Locate every uninfected red blood cell.
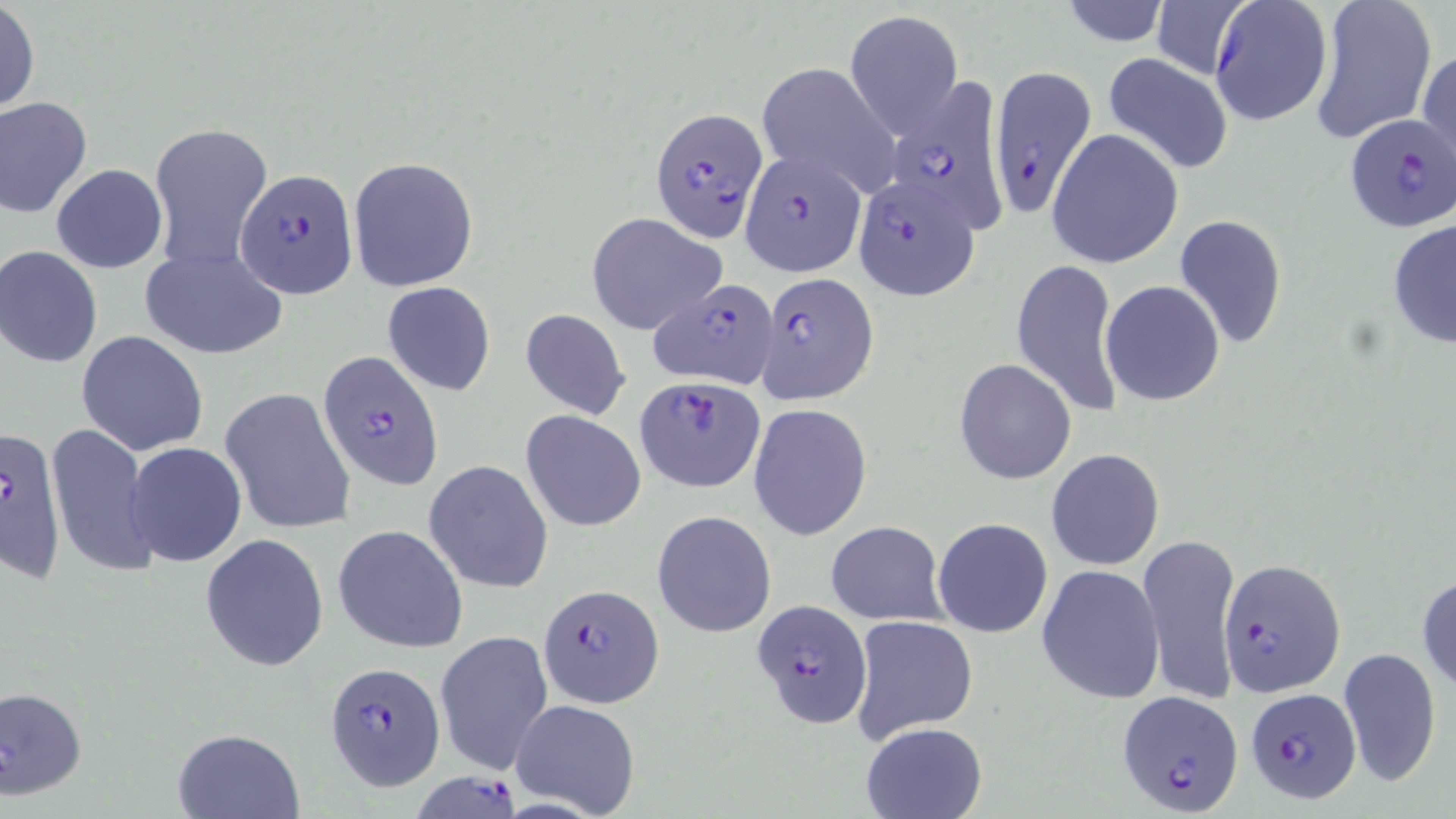
Approximate bounding boxes as (x1,y1)-(x2,y2) corner pairs in pixels.
Uninfected red blood cells (subset): (1054,0)-(1172,47), (1150,0)-(1255,78), (1308,1)-(1437,144), (0,2)-(39,116), (845,10)-(963,139), (1417,47)-(1456,175), (1102,52)-(1234,175), (755,61)-(899,195), (0,96)-(93,217), (149,123)-(273,271), (1047,129)-(1185,269), (347,156)-(478,292), (51,164)-(167,273), (586,212)-(728,337), (1174,214)-(1288,349), (1386,218)-(1456,350), (0,246)-(102,367), (140,247)-(286,359), (1011,256)-(1124,418), (1100,280)-(1226,406), (382,281)-(497,397), (519,307)-(630,421), (76,332)-(209,457), (953,358)-(1076,485), (220,387)-(357,534), (748,403)-(872,542), (521,409)-(645,532), (45,423)-(158,578), (126,442)-(247,568), (1047,449)-(1164,570), (424,460)-(553,593), (653,511)-(776,636), (933,517)-(1053,638), (825,521)-(948,624), (334,524)-(468,653), (1136,532)-(1243,709), (199,533)-(329,672), (1036,563)-(1165,705), (1416,572)-(1456,696), (849,614)-(979,742), (435,630)-(554,775), (1337,646)-(1443,788), (2,684)-(88,800), (509,698)-(643,818), (861,722)-(987,819), (173,728)-(302,818).

Summary:
  - Plasmodium falciparum-infected red blood cell locations (subset): (1209,0)-(1333,127), (987,64)-(1095,219), (884,78)-(1012,232), (650,107)-(770,243), (1344,115)-(1456,232), (740,150)-(866,277), (237,168)-(357,297), (852,173)-(982,300), (755,273)-(877,404), (656,275)-(779,383), (317,350)-(442,489), (1,428)-(68,582), (1220,558)-(1346,696), (538,582)-(663,708), (751,600)-(872,728), (324,661)-(446,789), (1245,688)-(1362,805), (1117,689)-(1242,814), (412,763)-(528,819)
  - Slide-level diagnosis: Plasmodium falciparum
  - Magnification: 1000x
  - Image size: 1456×819 pixels
  - Field of view: one of a larger specimen
  - Modality: optical microscopy
  - Stain: May-Grünwald-Giemsa
  - Preparation: thin blood smear